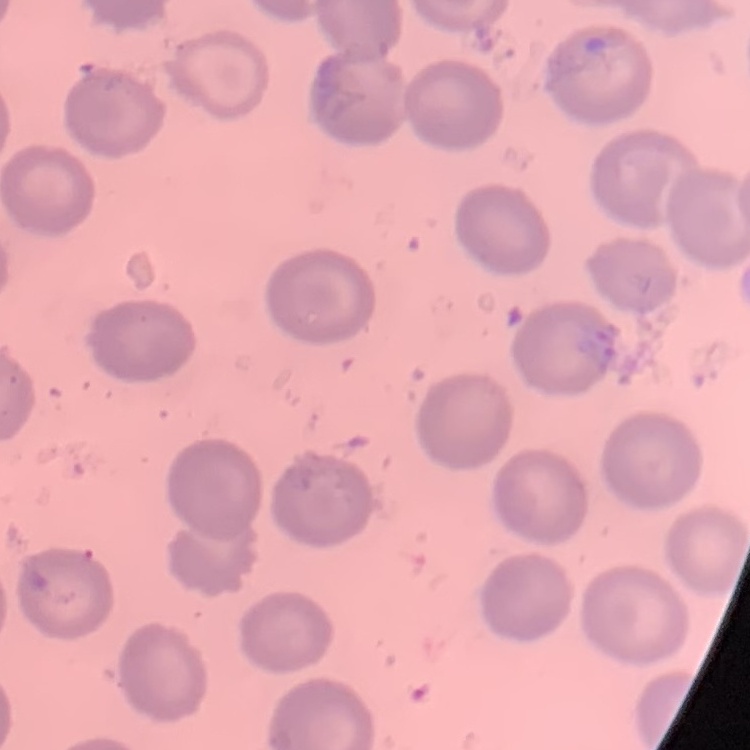
red blood cell morphology = no rouleaux formation
stain = Field's or Giemsa
preparation = thin blood film
image type = one tile cut from a larger photomicrograph